Outline each blood parasite and name the species.
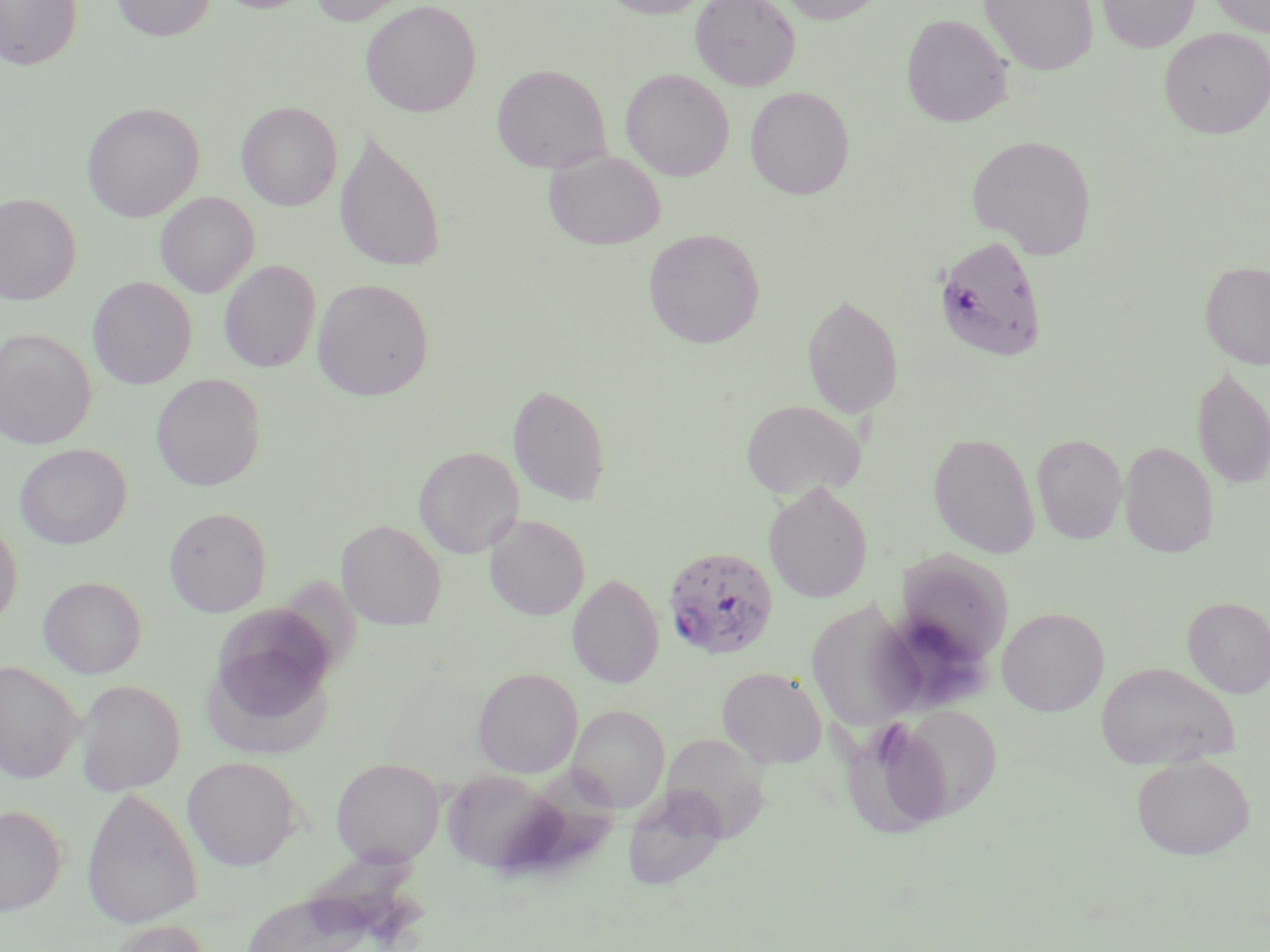
Approximate bounding boxes as [x1, y1, x2, y2] in pixels.
Plasmodium falciparum-infected red blood cells: [933, 234, 1048, 362], [662, 545, 779, 660].
No Plasmodium ovale, Plasmodium malariae, Plasmodium vivax, Babesia divergens, or Trypanosoma brucei observed.

{
  "slide_level_diagnosis": "Plasmodium falciparum",
  "preparation": "thin blood film",
  "image_size": "1270×952 pixels",
  "field_of_view": "one of a larger specimen",
  "stain": "May-Grünwald-Giemsa",
  "uninfected_red_blood_cell_locations": "approximate bounding boxes as [x1, y1, x2, y2] in pixels: [0, 0, 82, 70], [111, 0, 216, 41], [213, 0, 318, 14], [308, 0, 416, 26], [360, 0, 482, 117], [600, 0, 713, 18], [690, 0, 801, 91], [777, 0, 886, 25], [979, 0, 1098, 75], [1096, 0, 1199, 53], [1208, 0, 1270, 36], [901, 13, 1012, 127], [1159, 28, 1270, 138], [492, 64, 611, 174], [620, 68, 734, 181], [745, 86, 855, 199], [236, 101, 342, 211], [81, 102, 204, 222], [334, 129, 446, 273], [967, 134, 1097, 258], [543, 150, 666, 250], [155, 192, 259, 298], [0, 193, 82, 304], [643, 229, 765, 348], [219, 260, 321, 372], [1200, 261, 1270, 368], [87, 276, 196, 389], [312, 278, 434, 401], [801, 291, 904, 419], [0, 328, 97, 448], [1191, 364, 1270, 490], [150, 373, 266, 491], [507, 383, 611, 506], [740, 399, 866, 500], [927, 431, 1040, 558], [1031, 433, 1128, 544], [1119, 441, 1218, 558], [15, 444, 131, 549], [414, 446, 524, 557], [764, 482, 873, 603], [164, 507, 272, 616], [484, 515, 590, 620], [0, 519, 22, 630], [337, 519, 447, 630], [895, 550, 1015, 665], [277, 573, 366, 683], [567, 574, 664, 688], [38, 576, 147, 678], [809, 593, 925, 731], [1182, 596, 1270, 698], [997, 608, 1109, 716], [204, 610, 338, 756], [0, 661, 84, 783], [1095, 661, 1239, 770], [473, 667, 583, 778], [717, 667, 826, 768], [74, 679, 186, 795], [893, 703, 1004, 822], [568, 705, 669, 812], [844, 719, 967, 843], [661, 732, 771, 841], [182, 755, 302, 870], [1131, 755, 1255, 860], [331, 757, 445, 866], [509, 765, 623, 877], [442, 768, 559, 875], [80, 786, 203, 929], [622, 791, 729, 892], [0, 804, 66, 915], [239, 890, 380, 951], [107, 919, 211, 952]",
  "magnification": "1000x",
  "modality": "optical microscopy"
}